Report the malaria status of this cell.
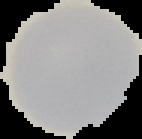
Uninfected.

From a thin blood smear. Image is 142×139 pixels. The area outside the segmented cell region is set to black.